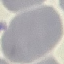
Summary:
  - Result: no malaria parasites seen
  - Preparation: thin blood film
  - Stain: Giemsa
  - Image type: automatically extracted cell patch, resized to 64 × 64 pixels
  - Capture: smartphone through the microscope eyepiece